Name the parasite shown.
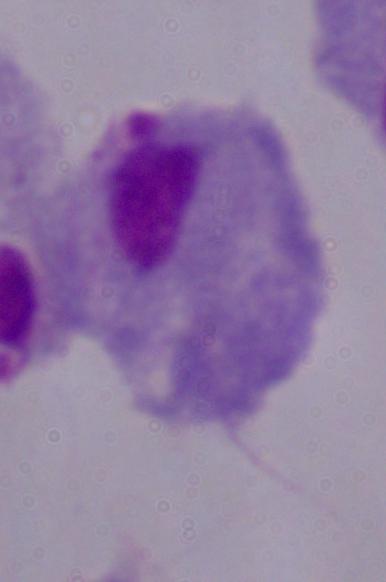
A trichomonad.

modality = micrograph
magnification = 1000x